Comment on the morphology of the red blood cells.
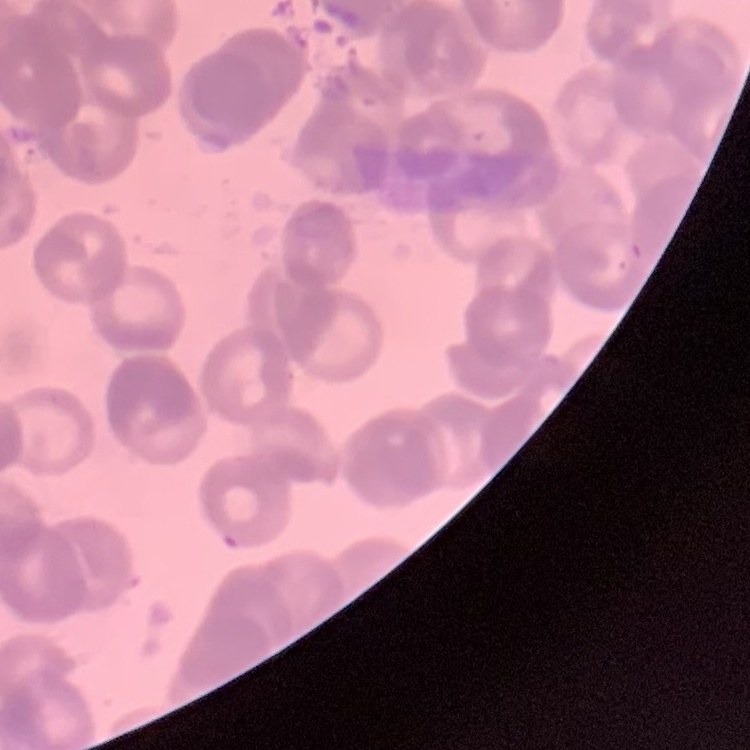

Rouleaux formation.

Field's or Giemsa stain. Thin blood smear. Square crop of a larger photomicrograph.